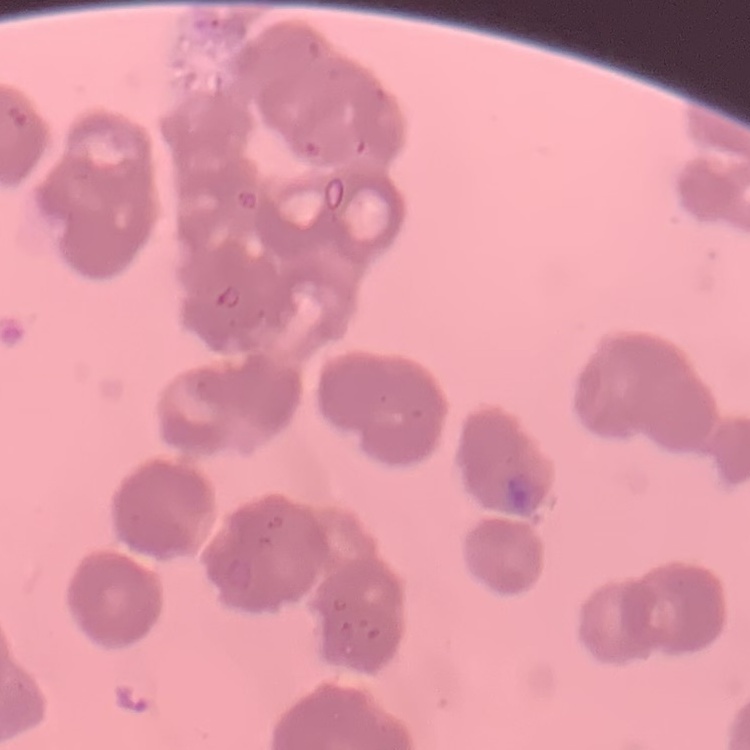
Summary:
  - Erythrocyte morphology: rouleaux formation
  - Preparation: thin blood smear
  - Image type: square crop of a larger photomicrograph
  - Stain: Field's or Giemsa